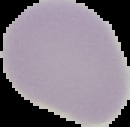
preparation: thin blood smear
image_type: cell region segmented out of the field of view; surrounding area masked to black
malaria_status: uninfected
image_size: 130×127 pixels